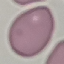
Result: no malaria parasites detected. Thin smear of blood. Photographed with a smartphone camera at the microscope eyepiece. Giemsa-stained preparation. Cell patch, automatically extracted from a larger field of view and resized to 64 × 64 pixels.